Point out each Plasmodium parasite.
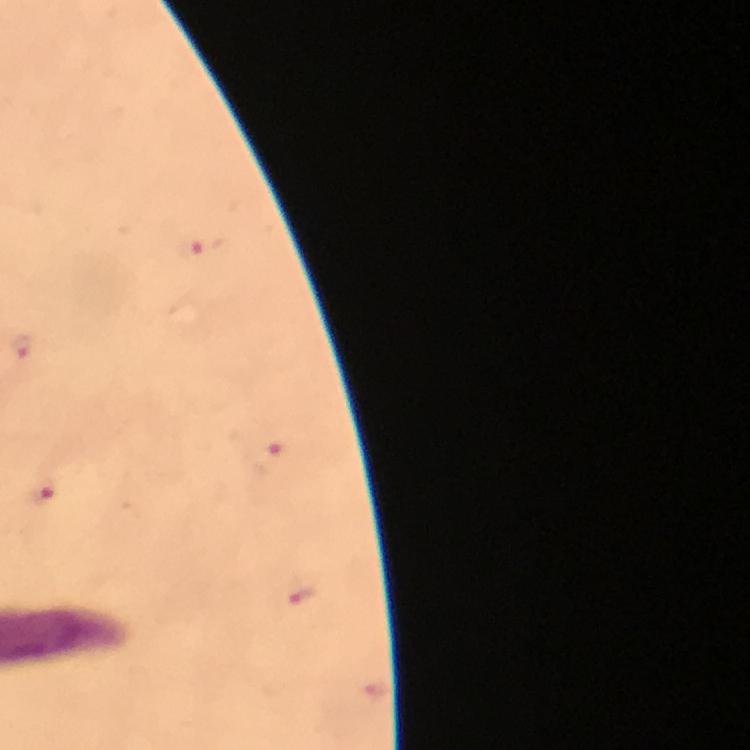
Approximate object centers, in pixels from the top-left corner.
Plasmodium parasites: (x=202, y=249), (x=20, y=346), (x=269, y=458), (x=42, y=492).

{
  "preparation": "thick blood film",
  "immersion_oil": "used",
  "cropped_from": "one field of view",
  "capture": "smartphone photograph through a microscope",
  "stain": "Giemsa",
  "image_size": "750×750 pixels",
  "context": "from a diagnostic examination for malaria",
  "magnification": "100x"
}